Outline each Plasmodium vivax-infected red blood cell.
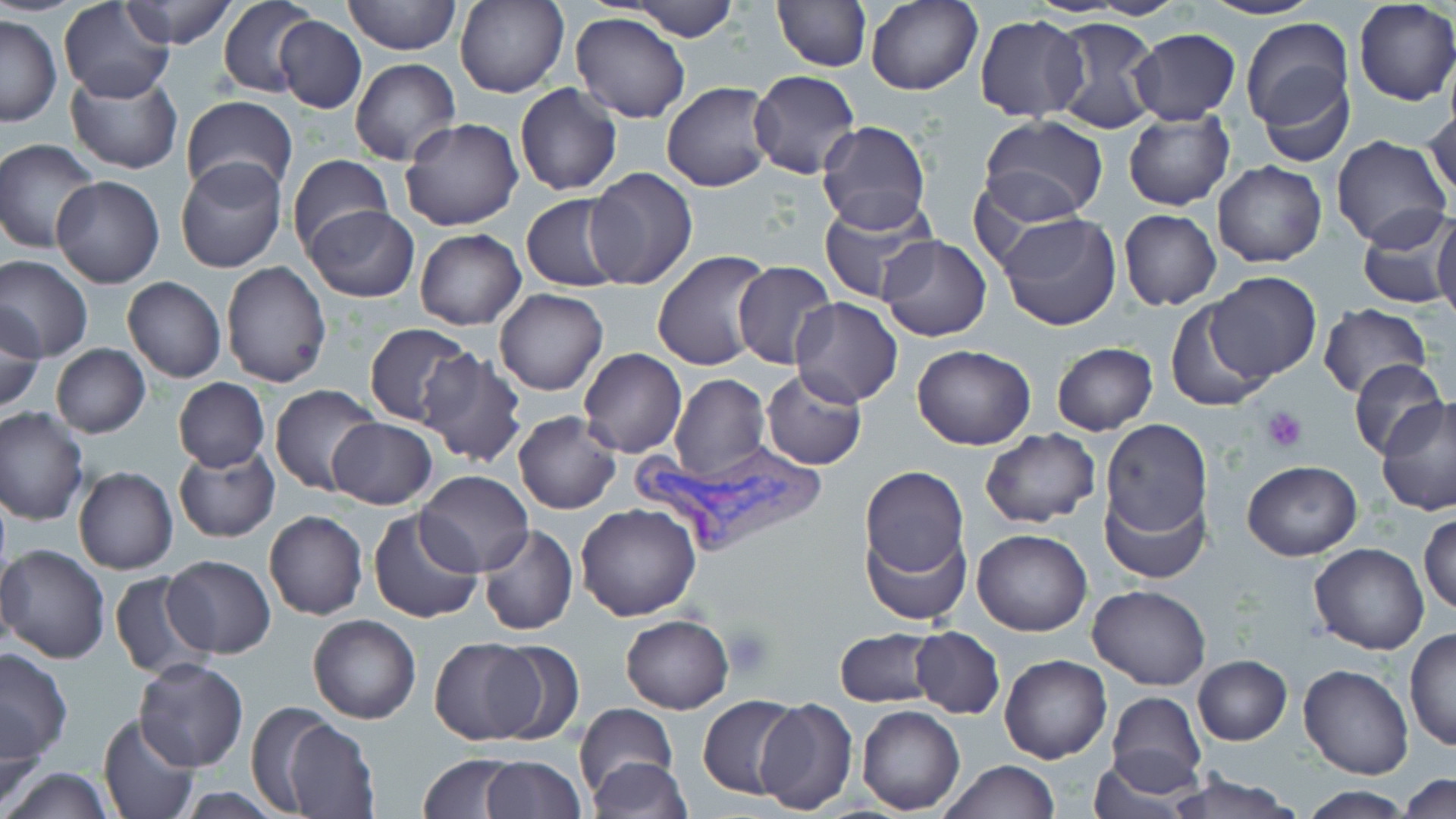

Approximate bounding boxes as (x1, y1, x2, y2) in pixels.
Plasmodium vivax-infected red blood cells: (626, 440, 826, 552).

Platelet locations: (1261, 407, 1310, 453), (722, 624, 775, 677). Uninfected red blood cell locations: (59, 0, 175, 102), (343, 0, 460, 54), (455, 0, 568, 98), (628, 0, 740, 41), (1082, 0, 1191, 19), (1198, 0, 1322, 21), (122, 1, 235, 49), (221, 1, 321, 99), (773, 1, 869, 71), (865, 1, 983, 96), (1352, 3, 1454, 106), (570, 13, 691, 123), (1, 15, 62, 127), (975, 15, 1087, 121), (275, 17, 366, 112), (1046, 17, 1163, 134), (1239, 17, 1354, 137), (1129, 29, 1242, 126), (350, 58, 461, 167), (65, 66, 184, 175), (749, 69, 861, 178), (1258, 69, 1356, 168), (661, 81, 780, 192), (514, 82, 622, 196), (181, 95, 298, 202), (1423, 102, 1456, 205), (1122, 110, 1234, 211), (980, 115, 1109, 223), (399, 117, 524, 232), (816, 120, 931, 233), (1332, 136, 1451, 250), (1, 138, 100, 253), (286, 154, 391, 258), (175, 157, 287, 274), (1212, 162, 1327, 267), (585, 168, 697, 288), (50, 173, 166, 288), (522, 193, 630, 293), (819, 197, 940, 304), (303, 205, 419, 303), (1118, 209, 1221, 310), (1355, 209, 1455, 309), (997, 212, 1123, 332), (1433, 212, 1456, 326), (414, 228, 526, 329), (878, 235, 991, 342), (652, 248, 776, 371), (0, 253, 93, 362), (731, 259, 836, 369), (221, 260, 333, 389), (1205, 272, 1322, 382), (122, 277, 226, 382), (494, 287, 608, 396), (790, 297, 903, 407), (1165, 304, 1271, 413), (1317, 304, 1433, 399), (1, 306, 46, 414), (364, 323, 476, 427), (1051, 342, 1158, 435), (50, 343, 151, 437), (913, 345, 1037, 449), (578, 348, 687, 458), (26, 349, 141, 502), (419, 349, 526, 467), (1348, 357, 1446, 460), (760, 367, 867, 470), (669, 374, 769, 485), (172, 377, 270, 471), (268, 384, 383, 496), (1377, 395, 1454, 518), (1, 407, 89, 527), (513, 411, 621, 514), (327, 417, 436, 510), (1099, 419, 1213, 539), (978, 428, 1102, 529), (175, 446, 279, 543), (1240, 459, 1362, 561), (859, 465, 969, 582), (73, 466, 178, 575), (416, 469, 533, 577), (1096, 483, 1211, 587), (576, 502, 703, 621), (263, 510, 367, 620), (367, 510, 485, 624), (1419, 511, 1455, 618), (860, 516, 970, 628), (476, 524, 579, 636), (973, 529, 1091, 637), (1308, 542, 1431, 654), (0, 543, 112, 663), (2, 545, 29, 655), (162, 554, 276, 658), (110, 571, 213, 678), (1088, 583, 1211, 690), (308, 613, 421, 723), (620, 614, 734, 714), (908, 626, 1006, 718), (836, 628, 938, 706), (1404, 628, 1456, 753), (428, 636, 551, 744), (481, 637, 584, 743), (0, 647, 73, 762), (999, 654, 1111, 764), (1191, 654, 1292, 746), (133, 658, 250, 771), (1298, 663, 1414, 780), (1105, 690, 1206, 790), (697, 694, 803, 800), (754, 696, 857, 816), (572, 704, 678, 795), (858, 705, 965, 814), (1, 708, 50, 808), (97, 713, 202, 819), (275, 715, 379, 819), (419, 753, 521, 818), (479, 754, 584, 818), (1086, 756, 1198, 818), (586, 757, 692, 818), (938, 759, 1058, 818), (2, 767, 116, 818), (1163, 771, 1299, 819), (1401, 771, 1455, 816), (1295, 786, 1418, 818). Slide-level diagnosis: Plasmodium vivax. Single field of view. May-Grünwald-Giemsa stain. Image is 1456×819 pixels. Light microscopy. Thin blood smear. Captured at 1000x magnification.